Give a bounding box for every Plasmodium parasite, every leukocyte, and every artifact (stain precipitate or debris).
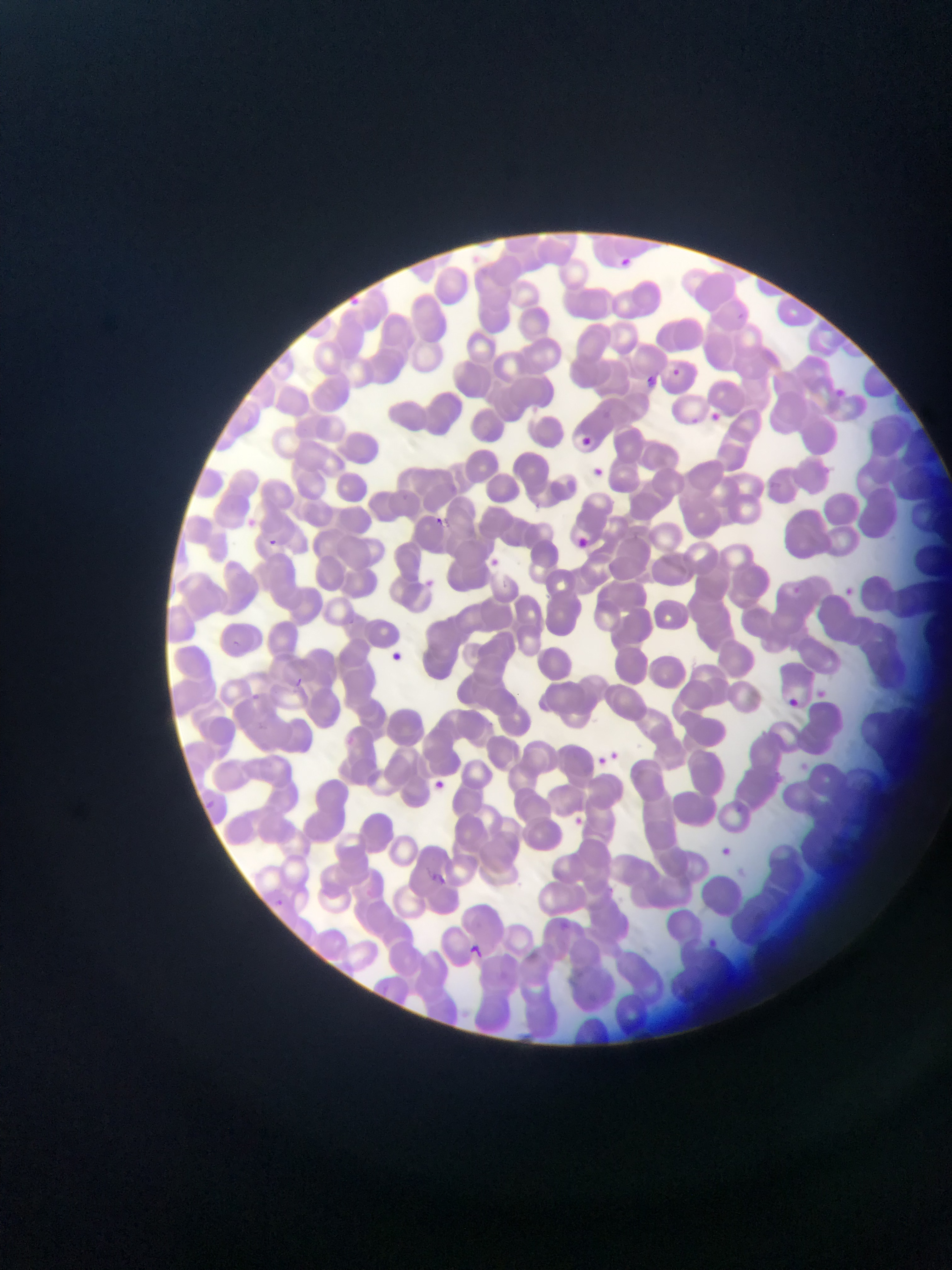
Approximate bounding boxes as [left, top, right, bottom] in pixels.
Plasmodium parasites: [611, 252, 637, 273], [351, 296, 360, 303], [736, 309, 751, 322], [668, 365, 683, 381], [639, 373, 659, 392], [706, 408, 725, 425], [574, 433, 596, 451], [586, 464, 605, 482], [429, 513, 448, 531], [571, 533, 591, 552], [259, 536, 282, 555], [482, 554, 502, 572], [788, 583, 804, 599], [837, 583, 861, 604], [221, 636, 245, 659], [383, 649, 408, 670], [290, 675, 306, 691], [812, 686, 830, 702], [783, 695, 803, 714], [591, 748, 619, 770], [605, 749, 624, 766], [427, 777, 450, 797], [200, 797, 217, 812], [196, 800, 215, 818], [567, 812, 588, 831], [713, 842, 737, 863], [429, 872, 450, 888], [269, 895, 288, 912], [558, 915, 574, 934], [707, 935, 724, 948], [463, 942, 486, 963].
No leukocytes observed.

{
  "country": "Ghana",
  "image_size": "952×1270 pixels",
  "preparation": "thin blood smear",
  "capture": "mobile-phone photograph through a microscope",
  "field_of_view": "single"
}